Report the malaria status of this cell.
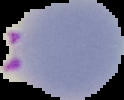

Parasitized.

Summary:
  - Preparation: thin blood film
  - Image size: 124×100 pixels
  - Image type: segmented cell region with the area outside set to black